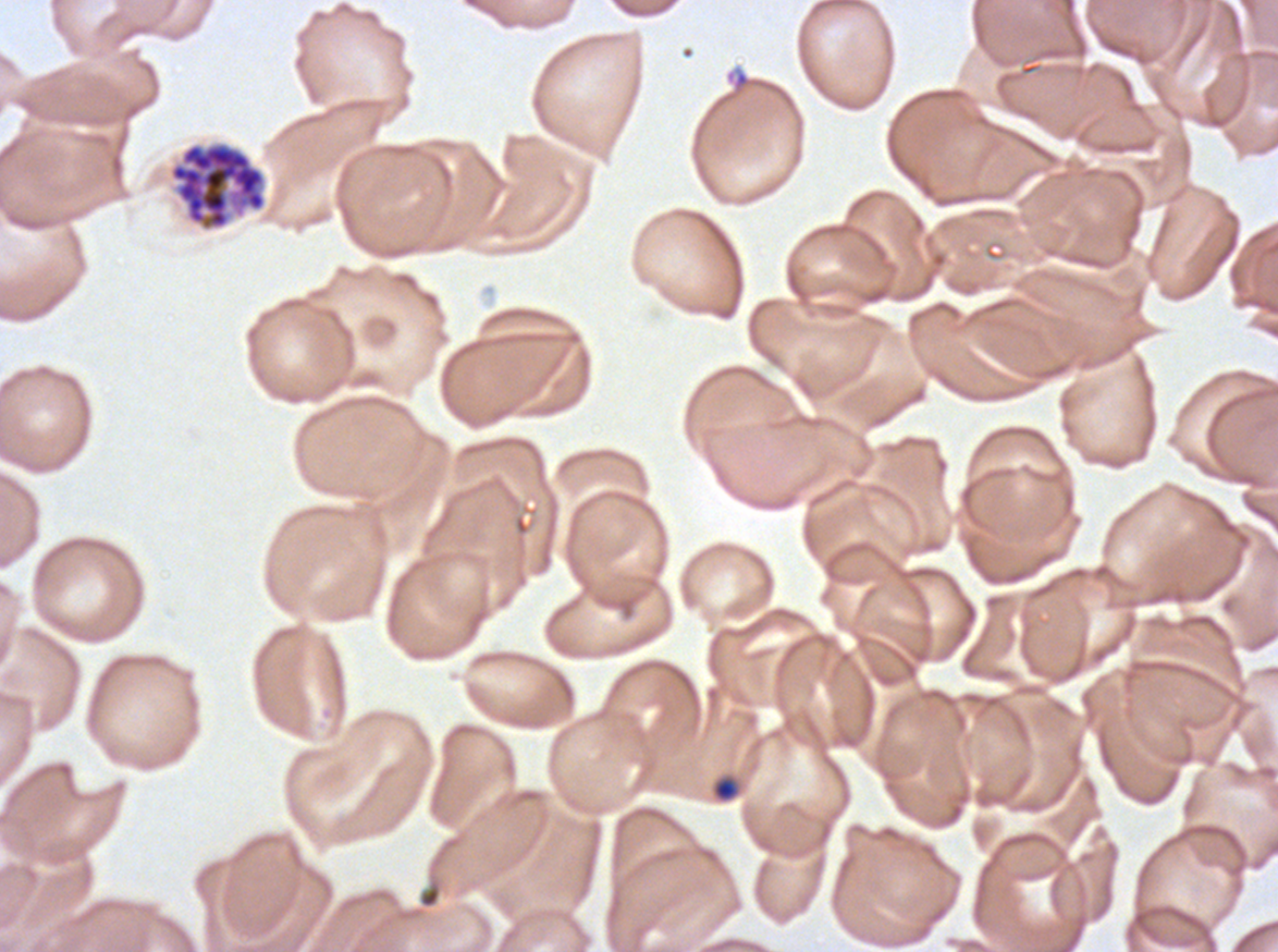
Approximate bounding boxes as [x1, y1, x2, y2] in pixels. Debris locations: [418, 883, 441, 909]. Late-ring/early-trophozoite locations: [711, 775, 741, 803]. Segmenter locations: [167, 140, 268, 233]. Ring locations: [725, 68, 753, 95]. Life-cycle stages observed: ring, late-ring/early-trophozoite, segmenter. Image is 1278×952 pixels. One sub-image of a larger composite. Ex-vivo Plasmodium falciparum culture from a patient in The Gambia, grown for 24 to 48 hours. Thin blood smear. Giemsa-stained preparation.